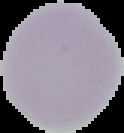

Summary:
  - Preparation: thin blood smear
  - Image type: cell region segmented out of the field of view; surrounding area masked to black
  - Malaria status: uninfected
  - Image size: 124×133 pixels